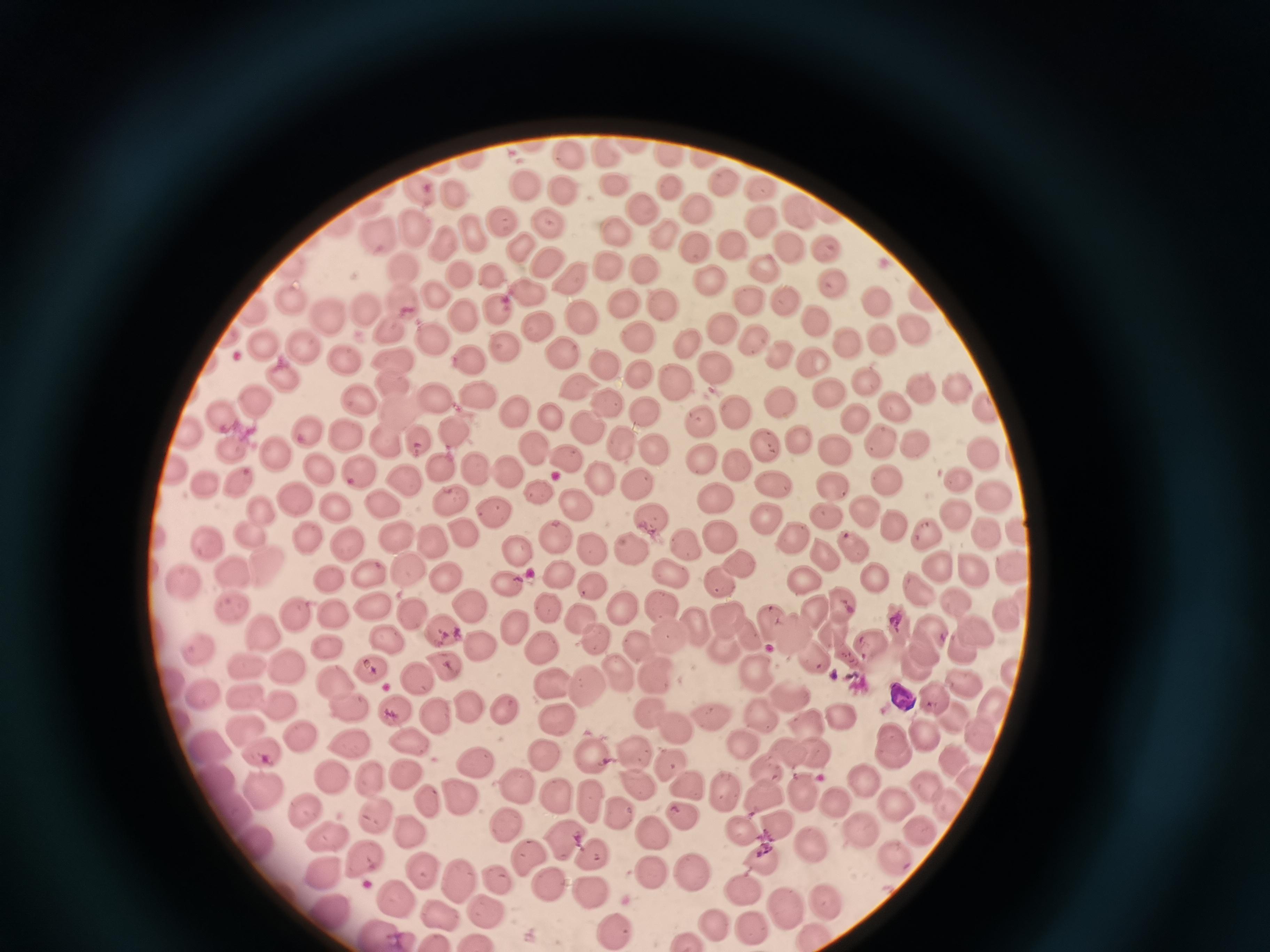

cell locations = approximate centers as [x, y] in pixels: [571, 152], [611, 152], [670, 157], [726, 182], [615, 184], [531, 188], [764, 188], [563, 189], [419, 191], [667, 191], [454, 192], [703, 208], [644, 209], [795, 209], [766, 218], [508, 220], [547, 220], [416, 226], [617, 229], [387, 234], [479, 234], [660, 235], [449, 243], [695, 246], [790, 246], [827, 246], [731, 247], [520, 249], [549, 261], [606, 263], [645, 263], [765, 267], [399, 268], [458, 273], [492, 273], [574, 275], [712, 281], [834, 282], [532, 289], [438, 293], [877, 296], [784, 298], [291, 299], [404, 300], [753, 300], [619, 304], [497, 305], [666, 306], [366, 307], [463, 315], [326, 316], [580, 318], [816, 318], [537, 323], [915, 325], [722, 327], [391, 330], [639, 336], [883, 337], [430, 340], [753, 340], [850, 340], [689, 344], [262, 345], [305, 345], [506, 345], [564, 350], [345, 356], [473, 356], [777, 356], [392, 357], [811, 362], [715, 364], [603, 365], [284, 374], [639, 374], [675, 381], [868, 381], [393, 382], [572, 384], [956, 388], [830, 390], [922, 390], [429, 394], [476, 396], [359, 401], [605, 401], [778, 402], [259, 403], [893, 405], [733, 407], [987, 409], [512, 410], [643, 411], [223, 412], [548, 415], [857, 419], [701, 421], [457, 427], [584, 429], [184, 430], [344, 431], [306, 435], [389, 440], [624, 440], [762, 440], [801, 440], [880, 440], [418, 443], [917, 444], [833, 445], [277, 446], [534, 446], [230, 447], [656, 450], [981, 451], [566, 457], [697, 457], [442, 462], [478, 464], [507, 465], [737, 467], [356, 469], [321, 473], [595, 475], [887, 476], [403, 479], [957, 479], [242, 482], [635, 483], [772, 483], [211, 484], [827, 484], [538, 491], [993, 493], [449, 499], [574, 499], [381, 501], [710, 501], [293, 502], [336, 505], [264, 506], [862, 507], [494, 509], [820, 511], [957, 514], [647, 515], [768, 516], [894, 523], [249, 528], [462, 529], [553, 530], [400, 533], [922, 533], [984, 534], [1019, 534], [429, 535], [792, 535], [720, 537], [304, 539], [347, 539], [205, 541], [850, 542], [686, 546], [594, 549], [821, 550], [516, 551], [632, 551], [264, 562], [1012, 562], [937, 563], [408, 567], [737, 567], [228, 569], [973, 569], [664, 571], [555, 572], [368, 575], [326, 576], [442, 576], [874, 576], [802, 579], [720, 580], [183, 581], [591, 581], [503, 584], [956, 599], [843, 601], [467, 604], [621, 604], [662, 604], [230, 607], [372, 608], [555, 611], [816, 612], [297, 613], [332, 613], [412, 617], [722, 617], [582, 619], [1005, 619], [695, 625], [772, 625], [443, 629], [513, 629], [974, 630], [932, 631], [670, 632], [262, 633], [834, 633], [790, 634], [388, 638], [594, 638], [750, 639], [872, 642], [197, 645], [540, 646], [326, 647], [475, 647], [726, 648], [923, 648], [961, 650], [811, 656], [249, 663], [281, 663], [914, 663], [445, 665], [372, 666], [655, 670], [752, 671], [1012, 672], [621, 676], [417, 678], [583, 682], [961, 682], [336, 684], [552, 685], [199, 693], [245, 695], [791, 697], [280, 698], [350, 705], [993, 705], [466, 706], [507, 707], [395, 710], [648, 711], [764, 713], [706, 715], [844, 717], [558, 718], [434, 719], [802, 719], [674, 723], [249, 727], [300, 733], [920, 735], [980, 735], [352, 737], [403, 739], [207, 745], [742, 747], [890, 747], [597, 749], [633, 751], [267, 752], [782, 752], [545, 753], [815, 758], [949, 759], [476, 760], [674, 760], [766, 770], [405, 772], [331, 773], [214, 776], [973, 778], [930, 779], [863, 780], [640, 782], [264, 784], [372, 784], [514, 786], [688, 786], [727, 788], [805, 791], [429, 793], [762, 794], [456, 797], [556, 799], [590, 800], [837, 800], [896, 801], [236, 808], [950, 809], [303, 810], [615, 811], [373, 812], [680, 813], [502, 822], [410, 825], [777, 825], [652, 827], [856, 828], [743, 829], [917, 833], [328, 836], [561, 836], [810, 840], [253, 842], [526, 852], [593, 853], [896, 854], [758, 858], [363, 859], [322, 870], [425, 870], [653, 870], [695, 871], [454, 877], [496, 880], [550, 884], [740, 886], [589, 890], [824, 891], [396, 894], [782, 901], [490, 909], [440, 910], [325, 913], [712, 923], [749, 923], [620, 927], [382, 932], [816, 934], [685, 941]
field of view = single
stain = Giemsa
capture = smartphone through the microscope eyepiece
preparation = thin blood smear
image size = 1270×952 pixels